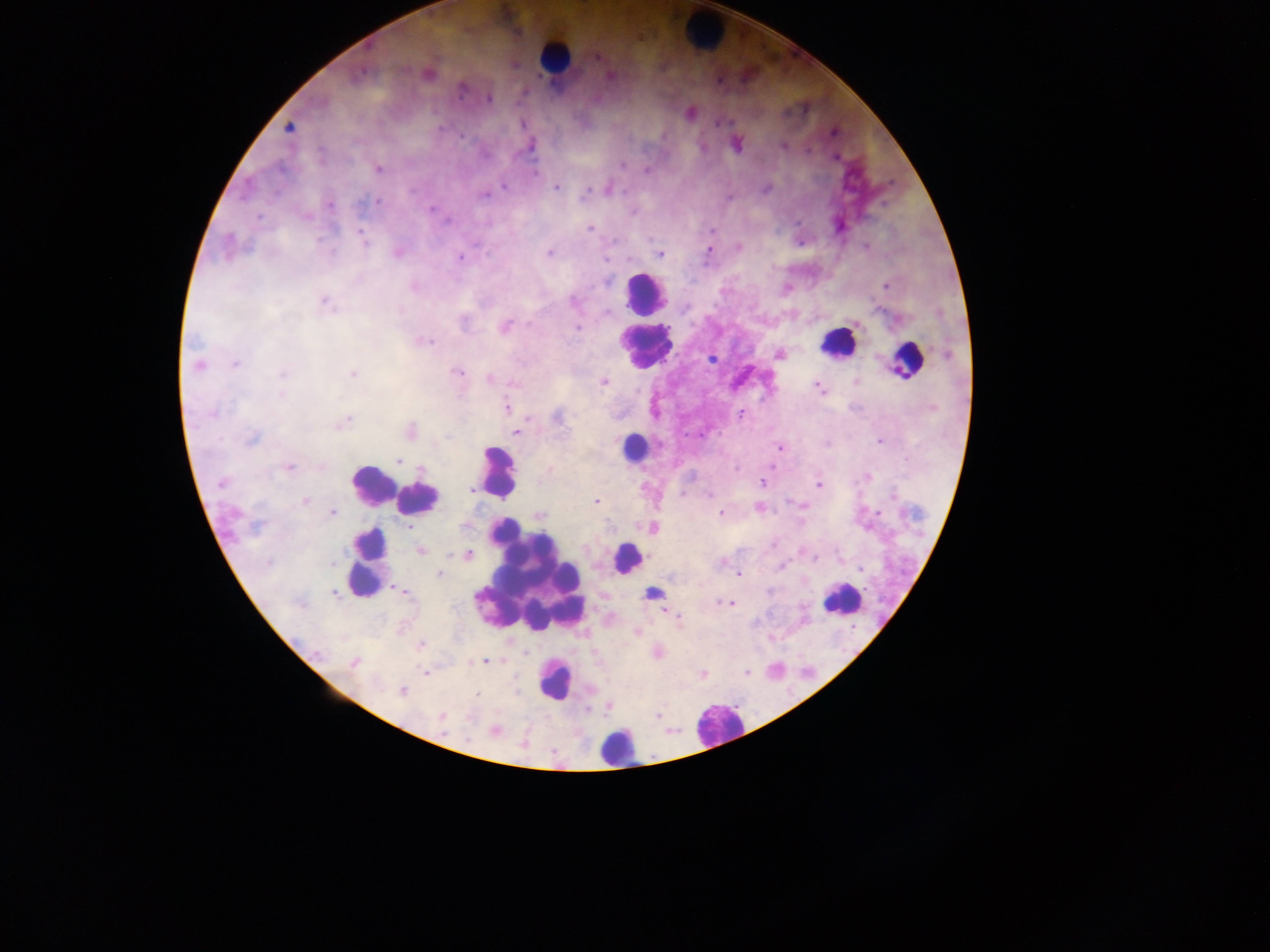
field of view = single
country = Ghana
leukocyte locations = approximate centers as x y in pixels: 703 31; 555 58; 644 291; 836 342; 644 347; 907 362; 634 447; 498 472; 371 484; 418 498; 626 559; 367 564; 526 577; 841 599; 555 682; 718 726; 616 747
preparation = thick blood smear
image size = 1270×952 pixels
capture = mobile-phone photograph through a microscope
Plasmodium parasite locations = approximate centers as x y in pixels: 598 57; 429 74; 608 77; 461 90; 489 99; 522 124; 288 127; 440 129; 833 133; 783 145; 530 147; 836 158; 621 166; 378 169; 647 170; 534 174; 503 186; 556 188; 586 191; 484 195; 377 201; 330 205; 432 209; 633 212; 258 217; 448 221; 590 229; 712 230; 362 236; 364 242; 739 247; 709 250; 398 252; 549 253; 660 254; 460 258; 607 282; 886 286; 414 287; 574 301; 324 302; 686 307; 607 312; 464 319; 505 326; 577 327; 427 342; 946 354; 779 355; 711 360; 235 364; 198 365; 457 372; 353 373; 282 374; 489 378; 855 381; 604 383; 817 386; 281 395; 507 408; 213 414; 740 414; 558 417; 342 422; 411 430; 515 432; 252 439; 879 442; 779 448; 399 460; 289 468; 421 469; 868 476; 762 483; 221 484; 819 485; 472 489; 709 494; 305 501; 596 501; 802 505; 759 507; 878 512; 332 513; 720 514; 539 516; 257 526; 653 527; 420 551; 468 554; 814 558; 269 563; 333 563; 861 569; 439 574; 738 574; 399 590; 334 593; 653 593; 725 603; 730 604; 678 618; 637 633; 421 645; 316 653; 485 661; 353 663; 426 672; 747 672; 703 675; 402 691; 477 695; 658 714; 442 716; 495 731